Assess the morphology of the red blood cells.
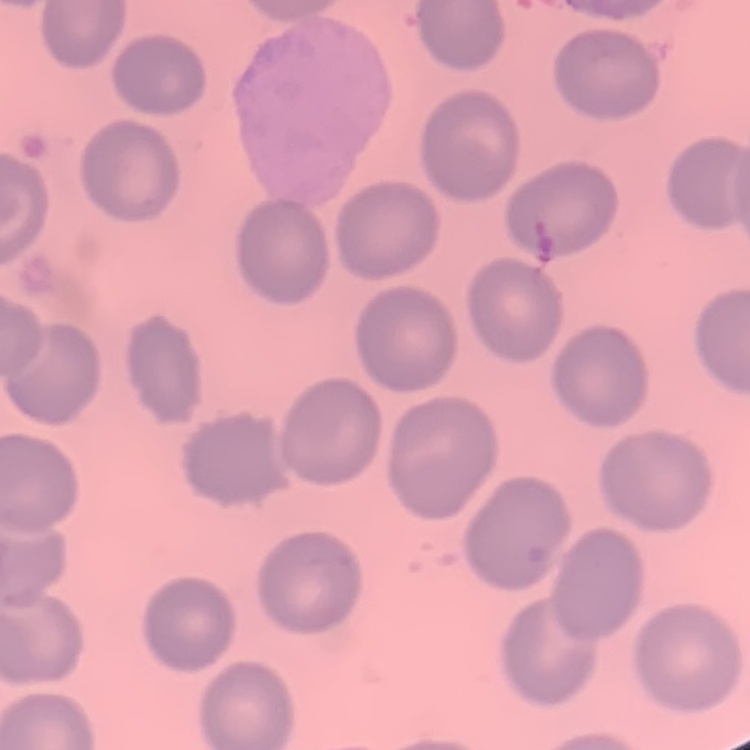

They show no rouleaux formation.

image type = one tile cut from a larger photomicrograph
stain = Field's or Giemsa
preparation = thin blood smear